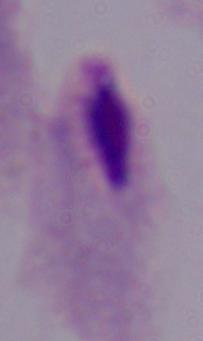
Micrograph. A trichomonad is shown. 1000x magnification.